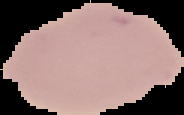
Image is 184×115 pixels. From a thin blood film. Cell region segmented out of the field of view; the surrounding area is masked to black. Malaria status: uninfected.